Give the position of every malaria parasite and every leukocyte.
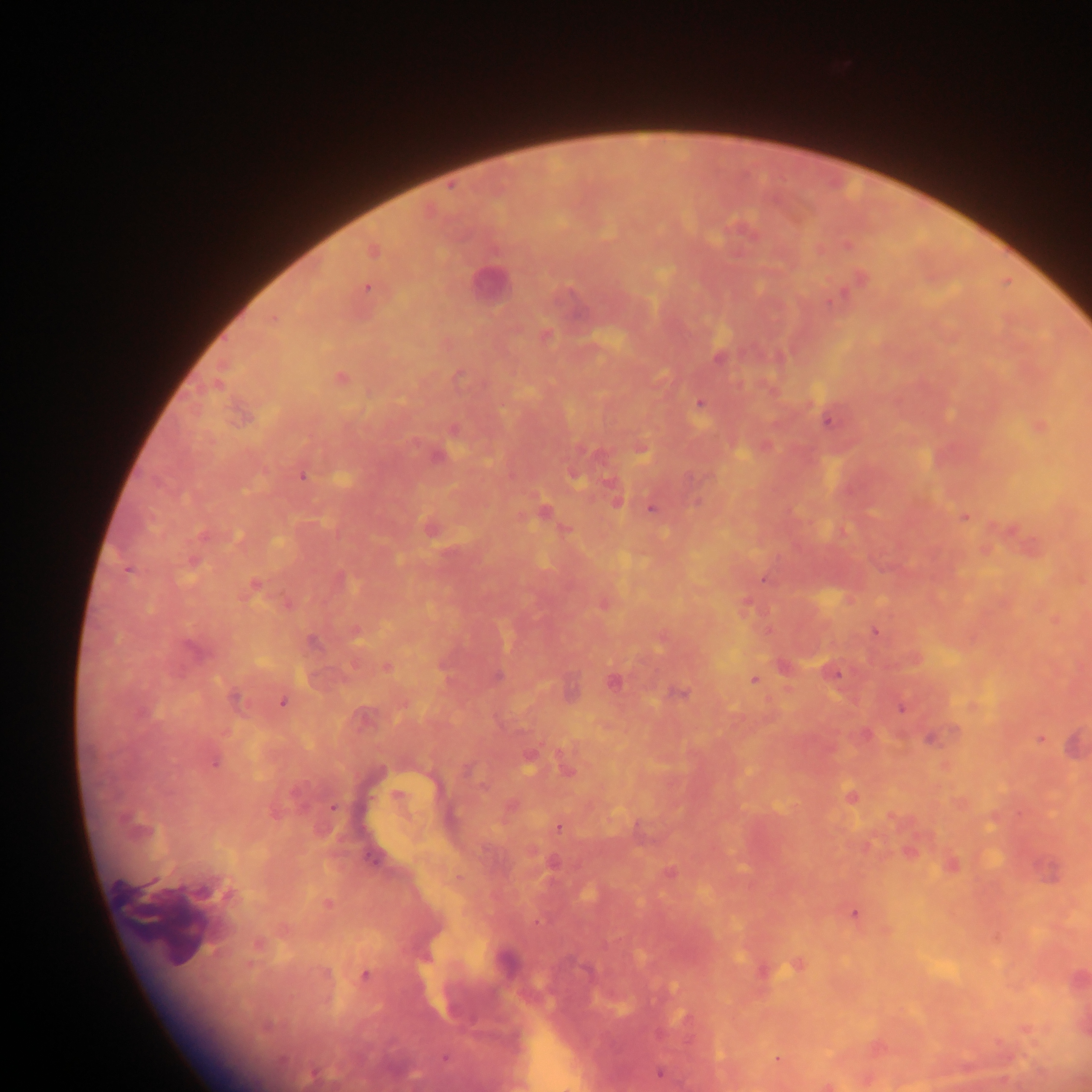
Approximate centers as {x, y} in pixels.
Malaria parasites: {848, 246}, {373, 251}, {861, 278}, {367, 287}, {840, 296}, {545, 335}, {719, 358}, {340, 377}, {699, 404}, {828, 422}, {437, 456}, {574, 476}, {302, 477}, {616, 501}, {652, 508}, {544, 511}, {964, 517}, {430, 528}, {193, 561}, {128, 570}, {764, 580}, {254, 586}, {746, 605}, {875, 632}, {355, 634}, {312, 643}, {191, 648}, {386, 668}, {835, 674}, {498, 676}, {754, 680}, {613, 682}, {680, 693}, {235, 698}, {282, 702}, {901, 709}, {1041, 739}, {930, 740}, {528, 760}, {215, 762}, {567, 770}, {850, 796}, {333, 808}, {559, 827}, {951, 865}, {669, 873}, {328, 902}, {855, 914}, {797, 965}, {365, 975}, {267, 1026}, {445, 1057}, {777, 1059}, {313, 1073}, {660, 1073}.
Leukocytes: {486, 283}, {163, 917}.

Summary:
  - Country: Ghana
  - Capture: mobile-phone photograph through a microscope
  - Image size: 1092×1092 pixels
  - Field of view: single
  - Preparation: thick blood smear